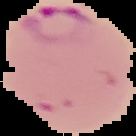

{
  "preparation": "thin blood smear",
  "image_type": "segmented cell region on a black background",
  "image_size": "136×136 pixels",
  "malaria_status": "parasitized"
}